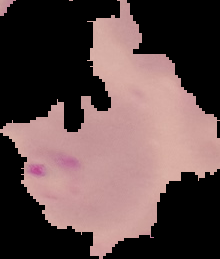
Summary:
  - Preparation: thin blood film
  - Image size: 220×259 pixels
  - Malaria status: parasitized
  - Image type: segmented cell region on a black background